Assess this cell for malaria.
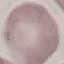

Uninfected.

Acquired by smartphone through the microscope eyepiece. Cell patch, automatically extracted from a larger field of view and resized to 64 × 64 pixels. Giemsa-stained preparation. Thin smear of blood.